Name the parasite shown.
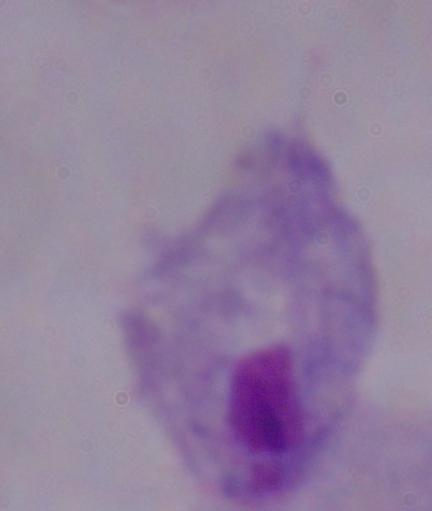

A trichomonad.

{
  "modality": "photomicrograph",
  "magnification": "1000x"
}